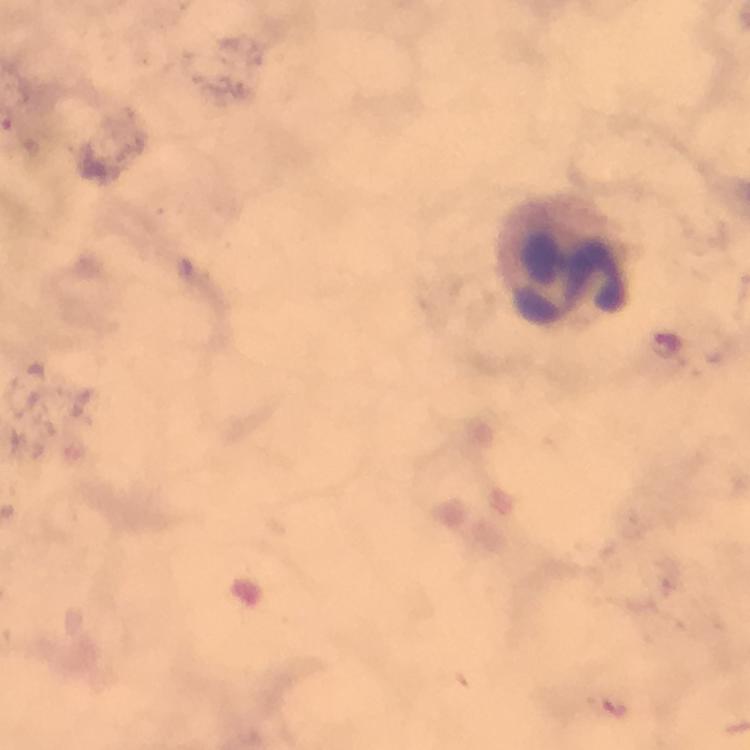
{
  "stain": "Giemsa",
  "capture": "smartphone camera through the microscope",
  "preparation": "thick blood film",
  "image_size": "750×750 pixels",
  "magnification": "100x",
  "cropped_from": "one field of view",
  "leukocyte_locations": "approximate object centers, in pixels from the top-left corner: (x=569, y=276)",
  "context": "from a malaria diagnostic workup",
  "immersion_oil": "used",
  "plasmodium_parasite_locations": "approximate object centers, in pixels from the top-left corner: (x=667, y=342)"
}